Assess this cell for malaria.
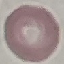
It is uninfected.

stain = Giemsa
capture = smartphone through the microscope eyepiece
preparation = thin blood film
image type = cell patch, automatically extracted from a larger field of view and resized to 64 × 64 pixels